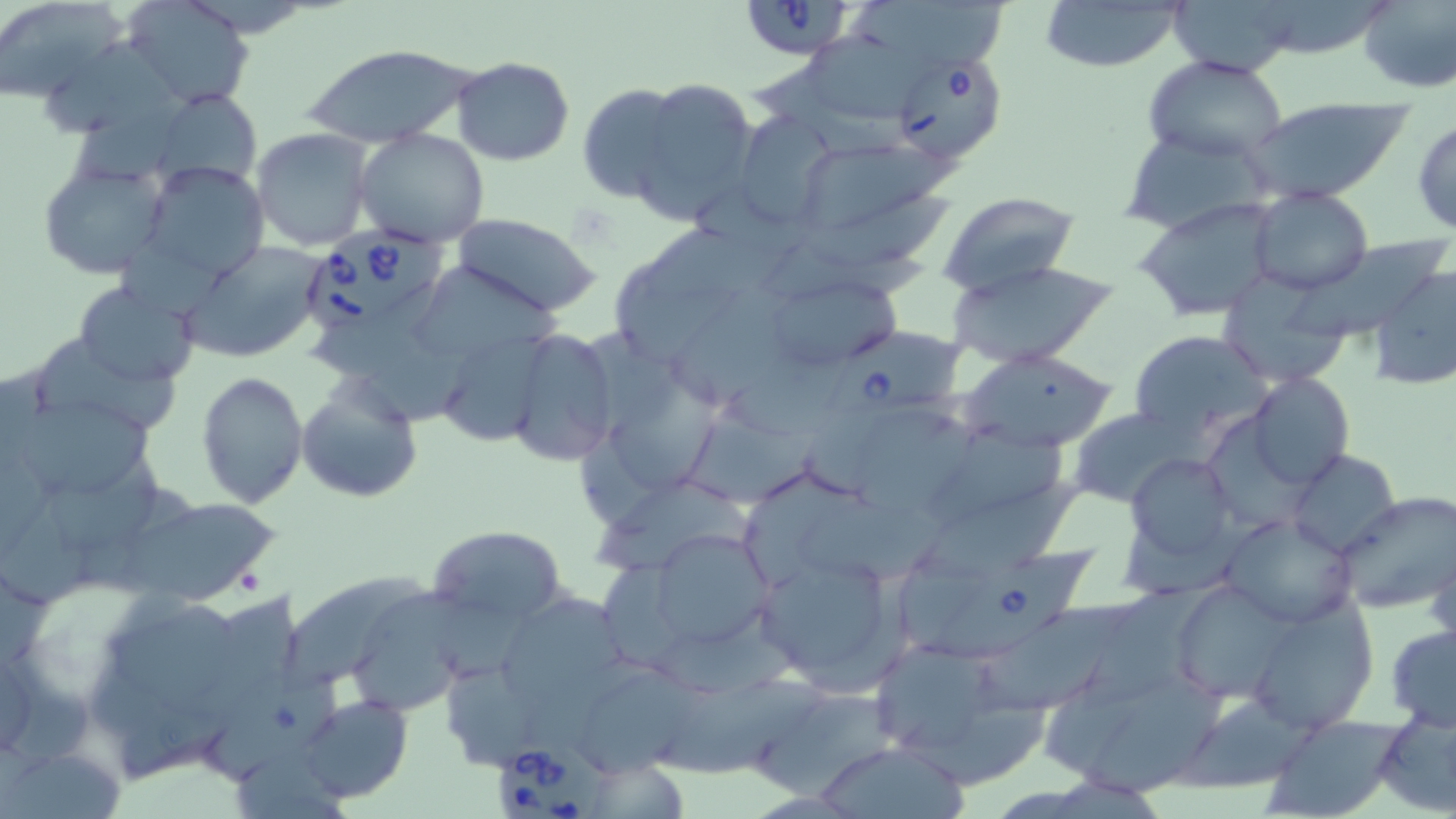

slide_level_diagnosis: Babesia divergens
preparation: thin blood smear
magnification: 1000x
modality: optical microscopy
uninfected_red_blood_cell_locations: 'approximate bounding boxes as [x1, y1, x2, y2] in pixels: [0, 0, 126, 105], [122, 0, 257, 111], [1033, 0, 1188, 71], [1355, 0, 1456, 93], [1169, 2, 1296, 75], [36, 41, 180, 137], [302, 43, 477, 147], [811, 44, 929, 119], [1144, 55, 1290, 163], [452, 57, 575, 166], [632, 78, 759, 222], [577, 85, 689, 202], [150, 88, 261, 190], [1248, 96, 1412, 202], [737, 112, 835, 220], [1412, 116, 1456, 237], [250, 127, 375, 251], [355, 128, 489, 246], [787, 139, 943, 244], [38, 158, 172, 280], [135, 161, 270, 285], [1249, 188, 1375, 295], [938, 193, 1080, 294], [1133, 197, 1286, 322], [451, 213, 601, 314], [1284, 237, 1451, 340], [182, 241, 329, 363], [947, 259, 1118, 368], [1367, 264, 1456, 392], [1217, 269, 1354, 387], [72, 280, 198, 386], [776, 280, 909, 365], [665, 283, 805, 418], [434, 324, 551, 446], [503, 327, 620, 468], [29, 328, 182, 442], [1129, 330, 1273, 440], [959, 349, 1120, 453], [194, 370, 308, 507], [295, 373, 423, 503], [1246, 373, 1354, 491], [16, 399, 159, 501], [681, 406, 823, 509], [1066, 407, 1200, 507], [1287, 449, 1401, 559], [1125, 451, 1240, 571], [911, 479, 1090, 577], [1333, 490, 1456, 615], [117, 494, 278, 602], [794, 499, 956, 584], [1220, 513, 1362, 627], [426, 524, 566, 629], [645, 528, 774, 654], [1427, 539, 1456, 655], [754, 550, 907, 694], [284, 577, 432, 696], [1168, 578, 1298, 704], [354, 591, 471, 713], [490, 591, 631, 718], [1242, 594, 1378, 731], [100, 603, 252, 719], [972, 605, 1143, 717], [1385, 623, 1456, 729], [206, 658, 348, 797], [653, 675, 833, 778], [1086, 686, 1234, 799], [297, 693, 413, 804], [756, 694, 903, 806], [1177, 695, 1316, 793], [898, 696, 1055, 792], [1370, 708, 1456, 817], [1262, 716, 1402, 818], [811, 740, 971, 817], [4, 745, 125, 818]'
babesia_divergens_infected_red_blood_cell_locations: 'approximate bounding boxes as [x1, y1, x2, y2] in pixels: [738, 0, 861, 57], [891, 52, 1008, 167], [299, 231, 445, 342], [817, 332, 971, 438], [922, 543, 1102, 664], [491, 740, 599, 819]'
image_size: 1456×819 pixels
stain: May-Grünwald-Giemsa
field_of_view: single